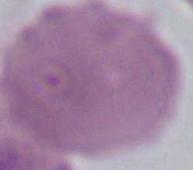
Photomicrograph. Captured at 1000x magnification. A red blood cell is seen.